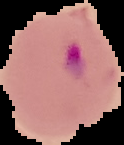

Summary:
  - Preparation: thin blood smear
  - Result: malaria parasites identified
  - Image size: 124×145 pixels
  - Image type: segmented cell region on a black background